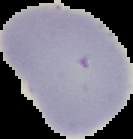
Summary:
  - Image type: segmented cell region with the area outside set to black
  - Preparation: thin blood film
  - Image size: 133×139 pixels
  - Malaria status: uninfected